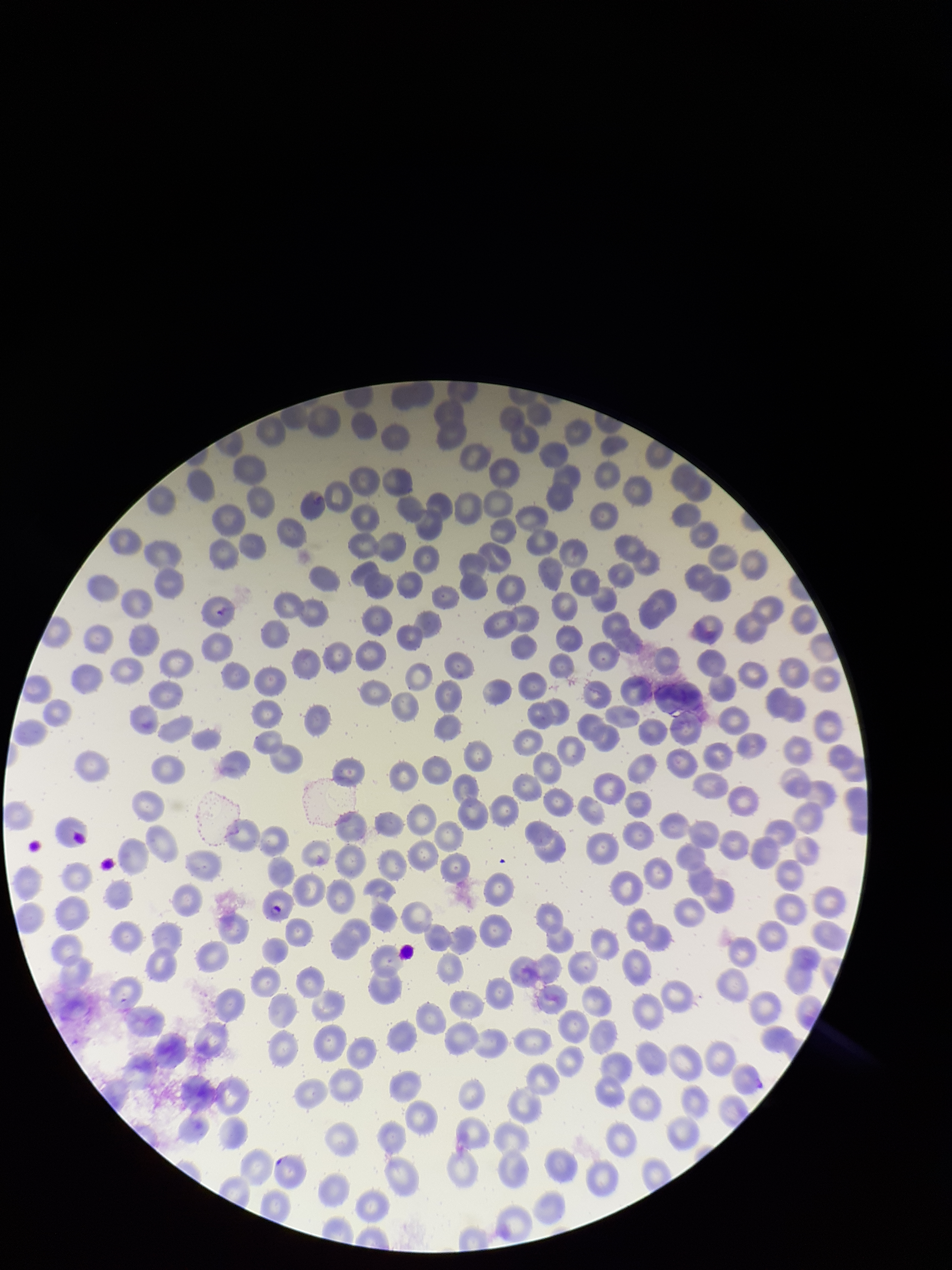

One field from this slide. Parasitized red blood cells: identified. Photographed through the microscope eyepiece with a smartphone camera. Red blood cell count: 255. Species reported for this patient: Plasmodium falciparum. Patient malaria status: infected. Giemsa stain. Image is 952×1270 pixels. Parasitized red blood cell count: 1. Preparation: thin.